Outline each blood parasite and name the species.
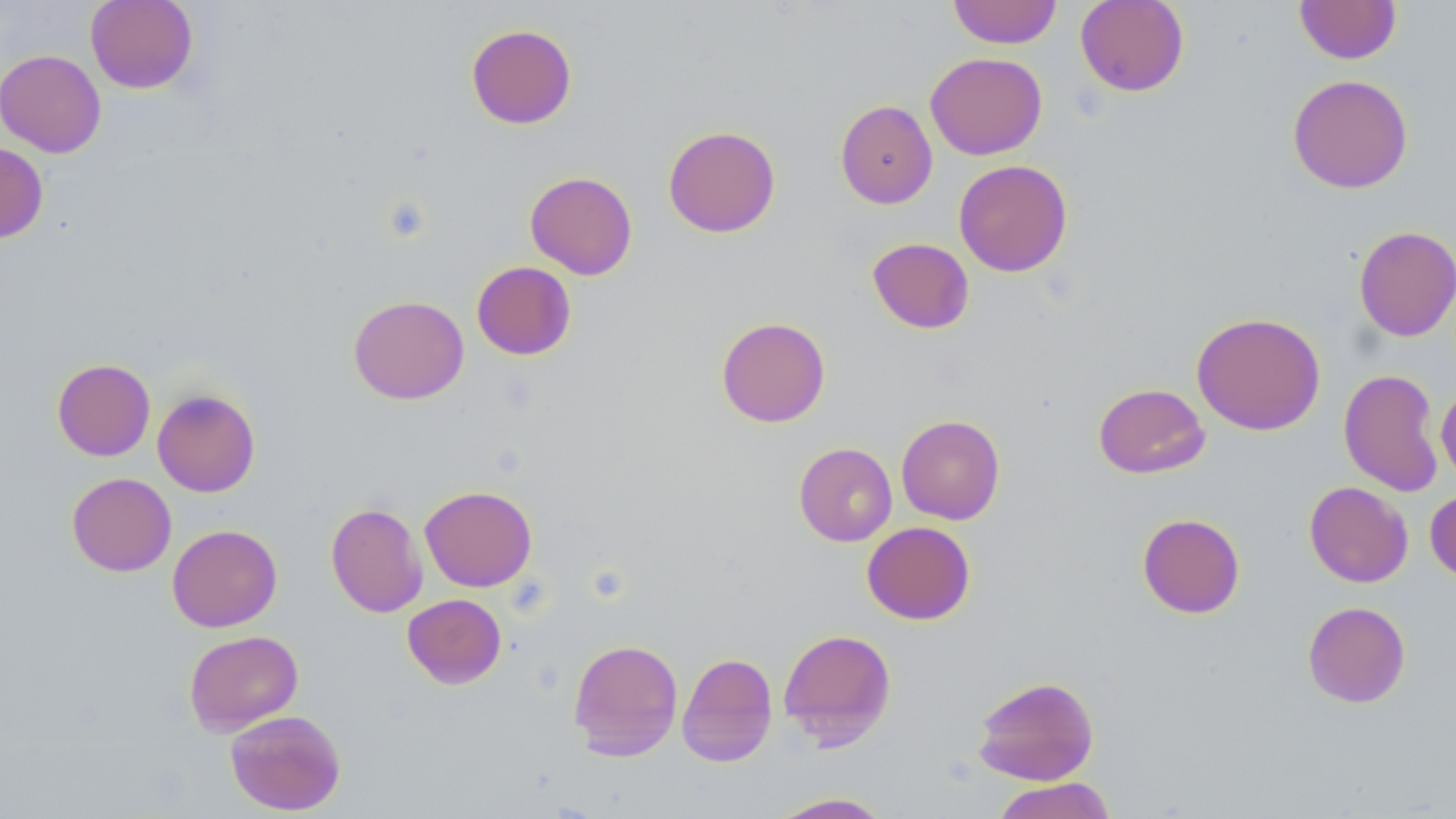

No blood parasites observed.

Approximate bounding boxes as named x1/y1/x2/y2 corners in pixels. Uninfected red blood cell locations: (x1=85, y1=0, x2=198, y2=94), (x1=948, y1=0, x2=1062, y2=48), (x1=1075, y1=0, x2=1189, y2=96), (x1=1294, y1=0, x2=1402, y2=64), (x1=465, y1=24, x2=577, y2=129), (x1=0, y1=49, x2=106, y2=157), (x1=925, y1=52, x2=1047, y2=159), (x1=1287, y1=74, x2=1413, y2=194), (x1=835, y1=99, x2=938, y2=208), (x1=663, y1=125, x2=781, y2=238), (x1=0, y1=142, x2=49, y2=244), (x1=954, y1=159, x2=1073, y2=277), (x1=525, y1=171, x2=638, y2=279), (x1=1353, y1=225, x2=1456, y2=341), (x1=867, y1=238, x2=974, y2=334), (x1=471, y1=261, x2=576, y2=360), (x1=348, y1=295, x2=469, y2=405), (x1=1191, y1=312, x2=1326, y2=435), (x1=716, y1=316, x2=831, y2=427), (x1=52, y1=358, x2=155, y2=461), (x1=1338, y1=368, x2=1445, y2=496), (x1=1093, y1=383, x2=1210, y2=479), (x1=1435, y1=384, x2=1456, y2=483), (x1=152, y1=389, x2=260, y2=497), (x1=896, y1=414, x2=1005, y2=525), (x1=794, y1=442, x2=897, y2=546), (x1=67, y1=472, x2=176, y2=576), (x1=1304, y1=481, x2=1413, y2=587), (x1=420, y1=485, x2=537, y2=592), (x1=1425, y1=488, x2=1456, y2=584), (x1=326, y1=502, x2=428, y2=617), (x1=1137, y1=513, x2=1245, y2=618), (x1=862, y1=521, x2=975, y2=625), (x1=167, y1=524, x2=282, y2=632), (x1=403, y1=594, x2=506, y2=688), (x1=1302, y1=601, x2=1411, y2=708), (x1=778, y1=628, x2=896, y2=748), (x1=183, y1=630, x2=304, y2=736), (x1=568, y1=638, x2=683, y2=761), (x1=677, y1=652, x2=778, y2=767), (x1=972, y1=675, x2=1100, y2=785), (x1=224, y1=709, x2=347, y2=815), (x1=991, y1=777, x2=1117, y2=819), (x1=767, y1=792, x2=895, y2=818). Slide-level diagnosis: no evidence of blood parasites. Light microscopy. Image is 1456×819 pixels. Thin blood film. May-Grünwald-Giemsa stain. One field of a larger specimen. 1000x magnification.